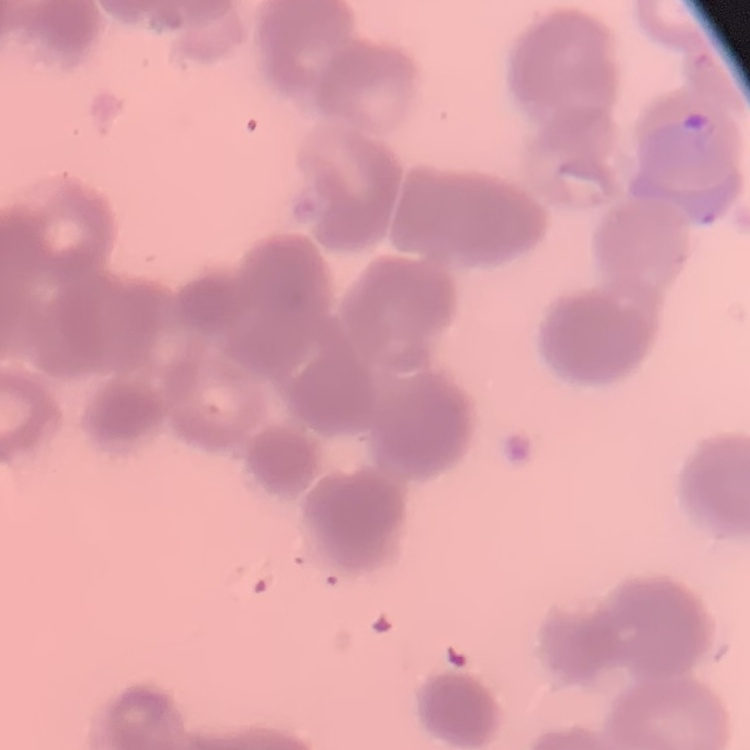

Summary:
  - Erythrocyte morphology: rouleaux formation
  - Image type: square crop of a larger photomicrograph
  - Preparation: thin blood smear
  - Stain: Field's or Giemsa